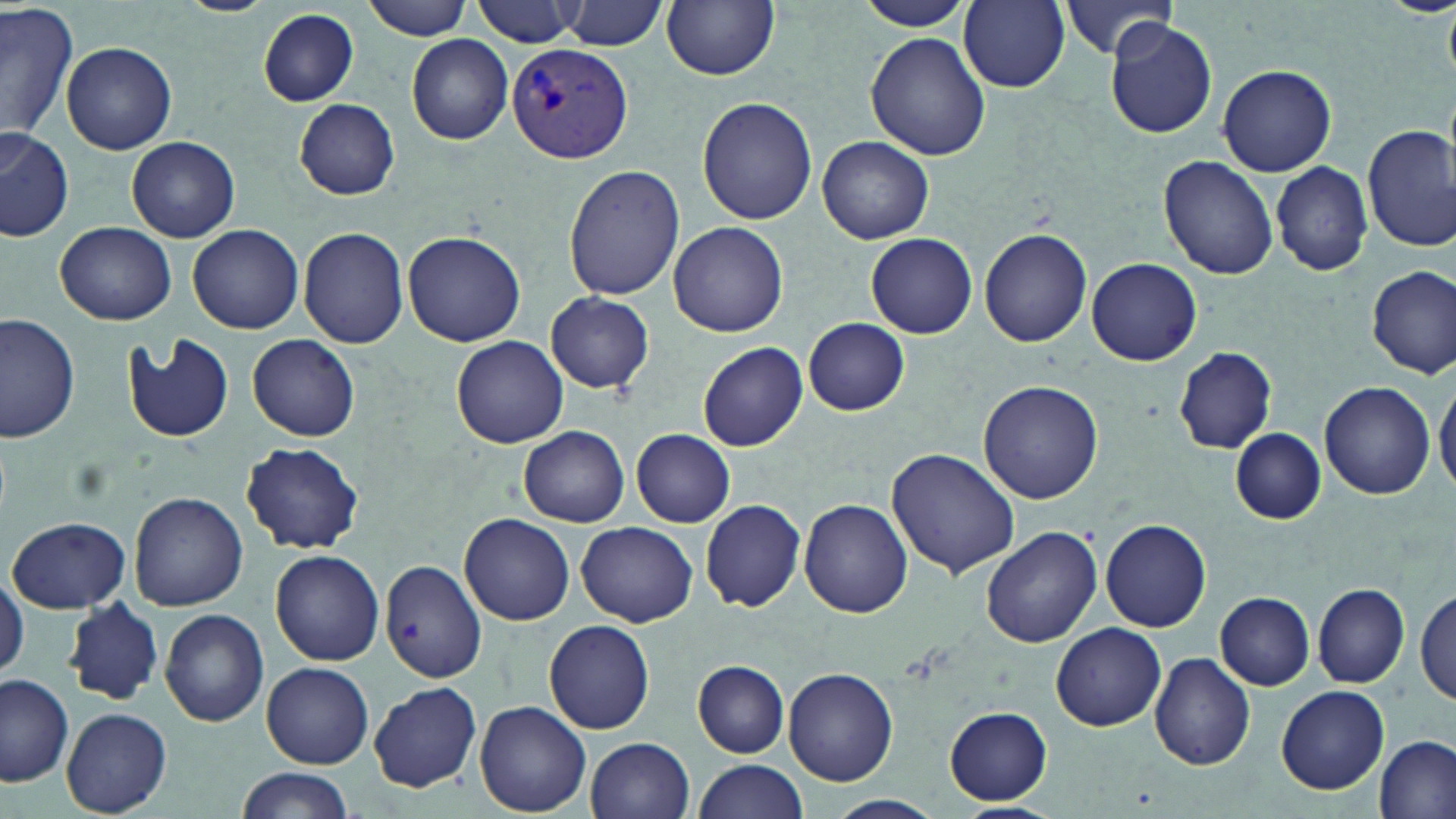 Approximate bounding boxes as [x1, y1, x2, y2] in pixels. Plasmodium vivax-infected red blood cell locations: [506, 44, 633, 166]. Uninfected red blood cell locations: [361, 0, 473, 40], [473, 0, 582, 47], [958, 0, 1069, 91], [562, 1, 667, 50], [662, 1, 780, 81], [858, 1, 979, 32], [1057, 1, 1182, 62], [0, 3, 77, 144], [257, 9, 358, 107], [1105, 19, 1217, 139], [866, 32, 990, 161], [407, 34, 513, 145], [62, 40, 176, 155], [1217, 63, 1338, 176], [698, 97, 817, 225], [295, 99, 400, 199], [1363, 123, 1456, 251], [0, 128, 74, 243], [818, 136, 934, 243], [126, 137, 239, 242], [1159, 155, 1278, 280], [1271, 159, 1374, 276], [563, 165, 685, 301], [668, 220, 788, 337], [55, 222, 176, 325], [188, 223, 304, 334], [298, 226, 408, 349], [978, 228, 1093, 348], [403, 230, 526, 347], [865, 233, 977, 339], [1085, 257, 1202, 365], [1368, 265, 1455, 378], [545, 292, 655, 394], [1, 315, 79, 444], [803, 318, 910, 416], [122, 333, 235, 444], [247, 333, 361, 440], [451, 336, 570, 448], [698, 342, 808, 452], [1173, 347, 1277, 453], [1434, 377, 1456, 497], [979, 380, 1105, 505], [1318, 381, 1435, 499], [518, 426, 629, 527], [1230, 427, 1326, 524], [631, 429, 736, 528], [240, 441, 364, 554], [886, 445, 1023, 578], [128, 491, 248, 610], [800, 498, 913, 618], [700, 499, 807, 612], [461, 513, 575, 625], [9, 516, 131, 611], [1101, 519, 1211, 632], [577, 522, 697, 627], [982, 527, 1103, 648], [270, 548, 386, 665], [379, 560, 487, 682], [0, 564, 27, 685], [1313, 582, 1409, 687], [1415, 587, 1454, 705], [1216, 592, 1314, 689], [64, 599, 164, 706], [160, 608, 269, 727], [544, 618, 655, 734], [1050, 622, 1166, 731], [1148, 653, 1257, 770], [692, 660, 789, 756], [262, 662, 374, 767], [783, 667, 899, 786], [0, 673, 75, 787], [370, 681, 482, 792], [1277, 685, 1390, 794], [475, 701, 592, 816], [944, 707, 1052, 805], [62, 708, 171, 816], [1375, 735, 1455, 819], [587, 736, 695, 818], [694, 758, 807, 819], [236, 766, 358, 819], [824, 795, 945, 819], [954, 803, 1065, 819]. Slide-level diagnosis: Plasmodium vivax. May-Grünwald-Giemsa-stained preparation. Captured at 1000x magnification. Single field of view. Optical microscopy. Thin blood smear. Image is 1456×819 pixels.